Classify this cell by malaria status.
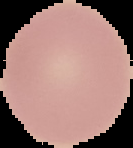
Uninfected.

Summary:
  - Image size: 133×148 pixels
  - Image type: segmented cell region with the area outside set to black
  - Preparation: thin blood film